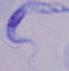
Summary:
  - Magnification: 1000x
  - Modality: micrograph
  - Identification: trypanosome